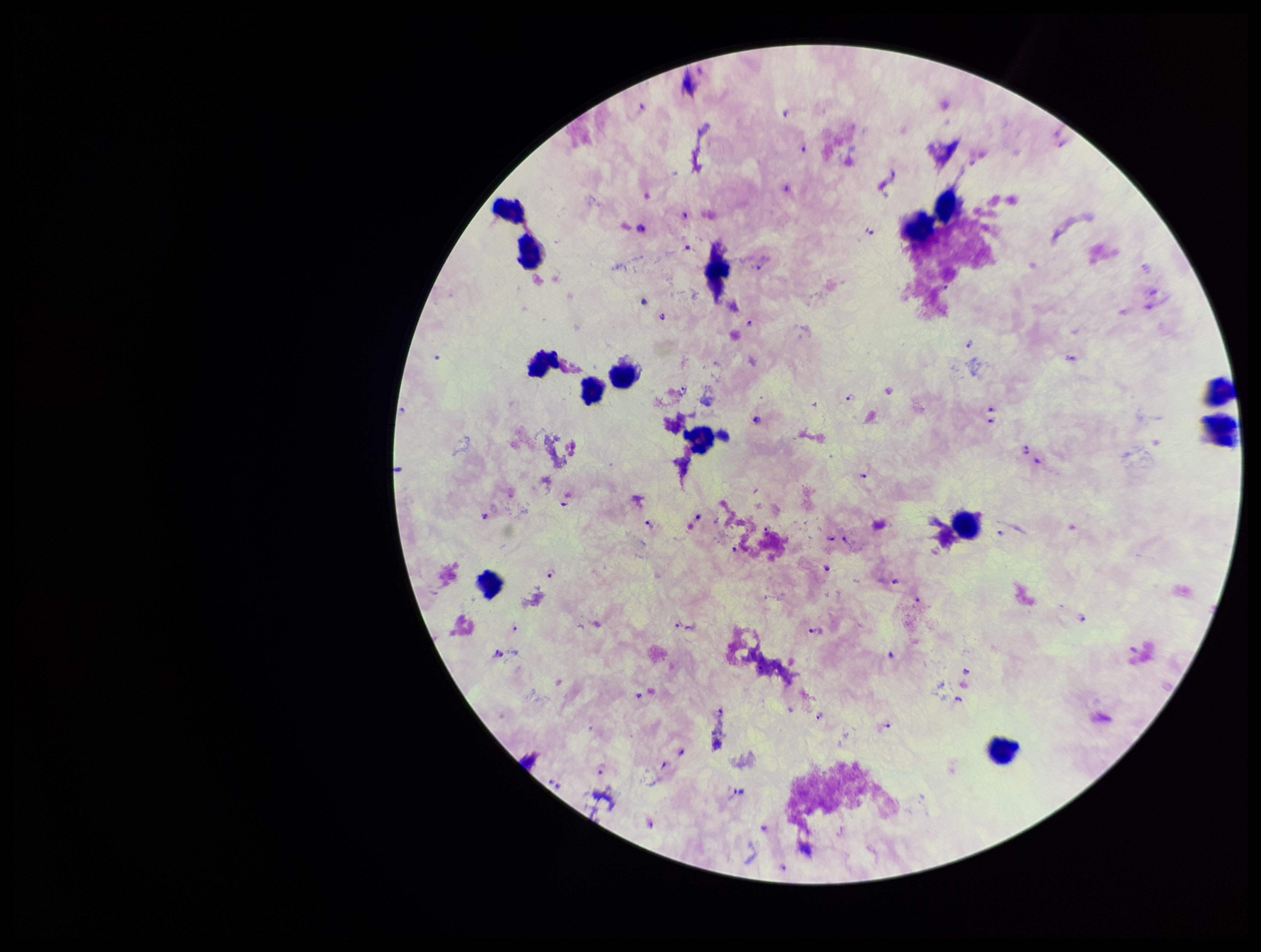

Photographed through the microscope eyepiece with a smartphone camera. Image is 1261×952 pixels. Species reported for this patient: Plasmodium falciparum. Single field of view. Preparation: thick smear. Giemsa stain. Patient malaria status: positive. Parasite count: 73. Leukocyte count: 14. Plasmodium parasites: identified.